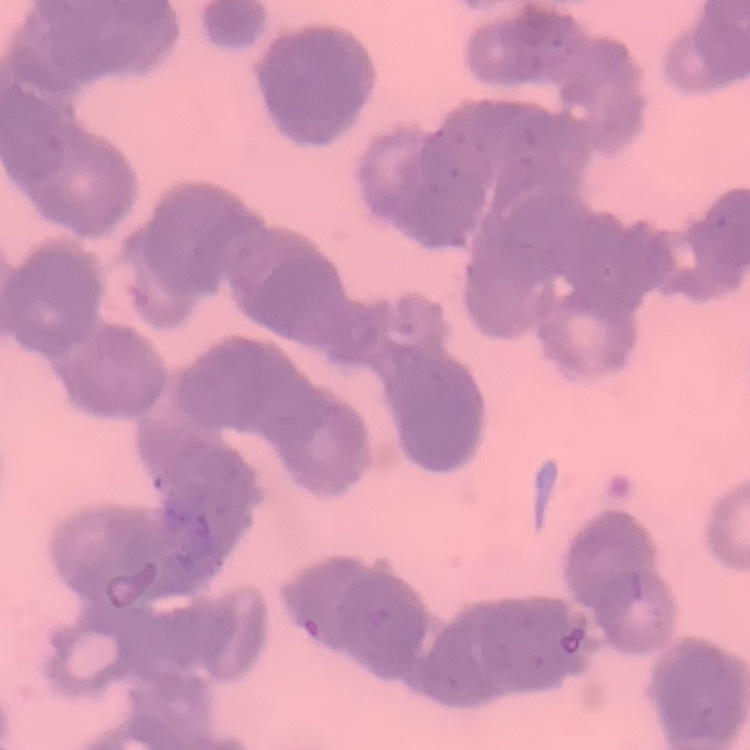

The erythrocytes exhibit rouleaux formation. Thin peripheral smear. Field's or Giemsa stain. Square crop of a larger photomicrograph.